Locate every malaria parasite and identify its life-cycle stage.
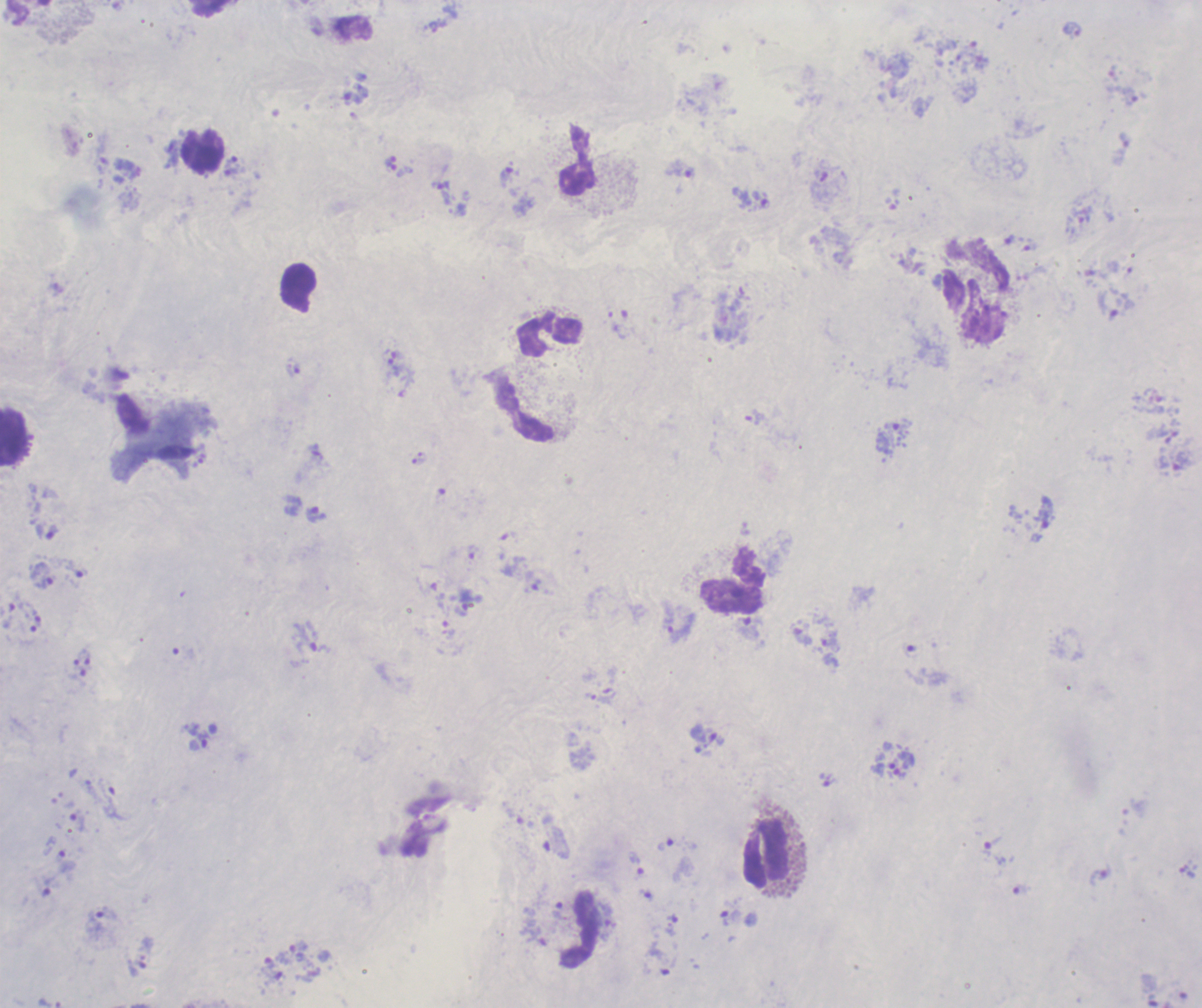

Approximate centers as [x, y] in pixels.
Trophozoites: [681, 169], [505, 177], [442, 193], [1029, 247], [293, 368], [754, 416], [892, 436], [316, 514], [52, 532], [78, 570], [45, 582], [749, 627], [679, 632], [801, 633], [309, 637], [195, 736], [827, 779], [77, 820], [555, 842], [665, 844], [991, 846], [635, 862], [1022, 889], [103, 914], [730, 917], [672, 925], [291, 951].
No schizont or gametocyte forms observed.

Approximate centers as [x, y] in pixels. Leukocyte locations: [204, 152], [577, 161], [976, 291], [549, 336], [524, 410], [13, 436], [732, 580], [765, 854], [580, 929]. Romanowsky-stained preparation. 100x magnification. Previously used in a real diagnosis. Image is 1202×1008 pixels. Thick blood film. One field from this slide. Background quality: poor.